Report the malaria status of this cell.
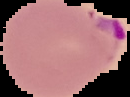
Parasitized.

image size = 130×97 pixels
preparation = thin blood smear
image type = segmented cell region on a black background